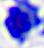

A leukocyte is seen. Photomicrograph. 400x magnification.